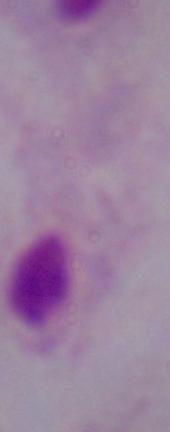
identification: trichomonad
magnification: 1000x
modality: photomicrograph